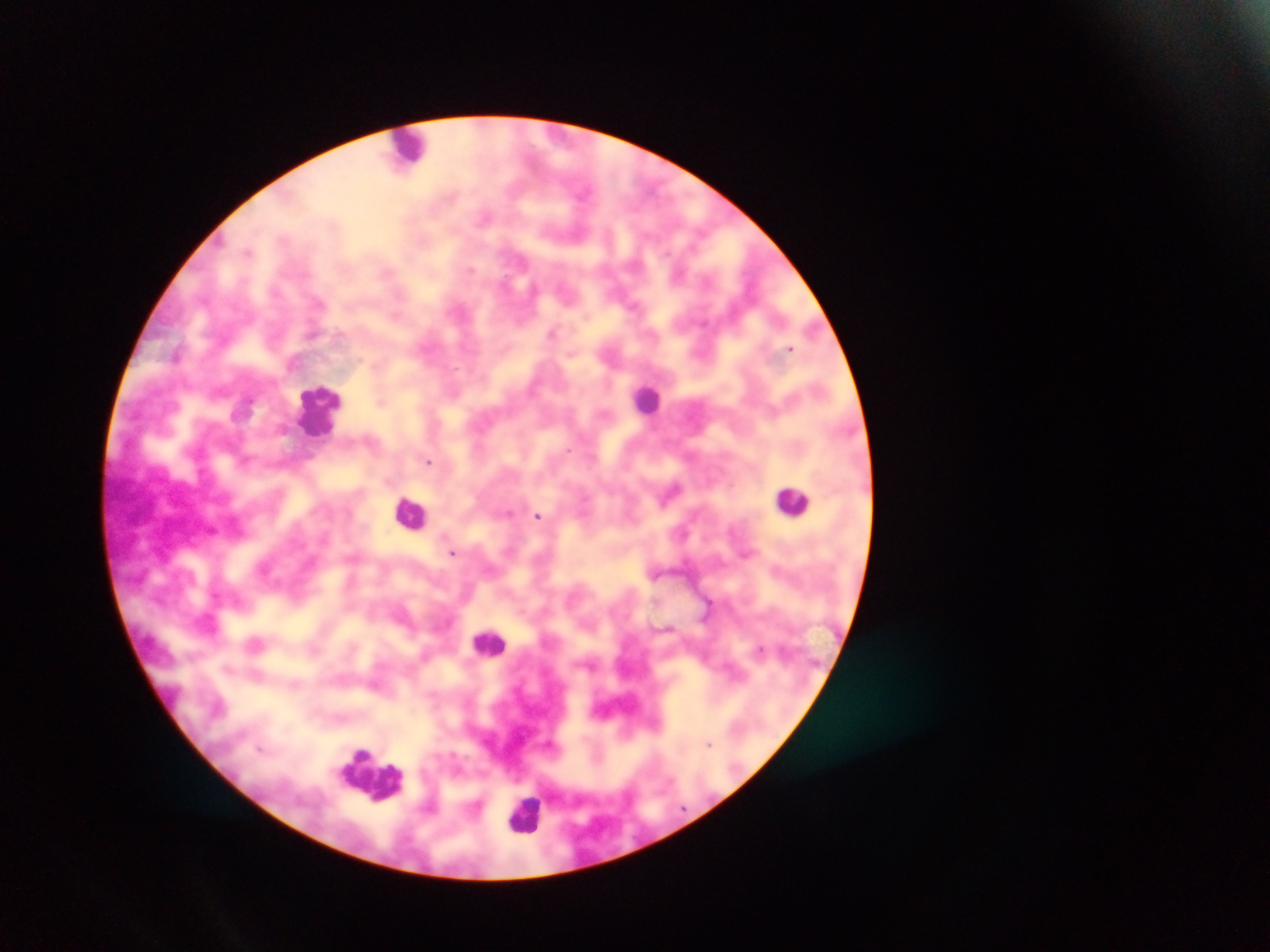
Approximate centers as [x, y] in pixels. Malaria parasite locations: [583, 192], [485, 218], [248, 251], [469, 270], [387, 271], [533, 289], [633, 305], [553, 332], [311, 335], [791, 348], [571, 354], [381, 402], [283, 429], [569, 450], [428, 461], [673, 489], [508, 512], [538, 516], [683, 533], [453, 552], [708, 601], [760, 649], [295, 685], [709, 743], [261, 748]. Leukocyte locations: [409, 148], [646, 398], [320, 407], [793, 501], [412, 512], [490, 643], [373, 775], [525, 812]. Collected in Ghana. Single field of view. Thick blood smear. Photographed through a microscope with a mobile-phone camera. Image is 1270×952 pixels.